Assess the morphology of the erythrocytes.
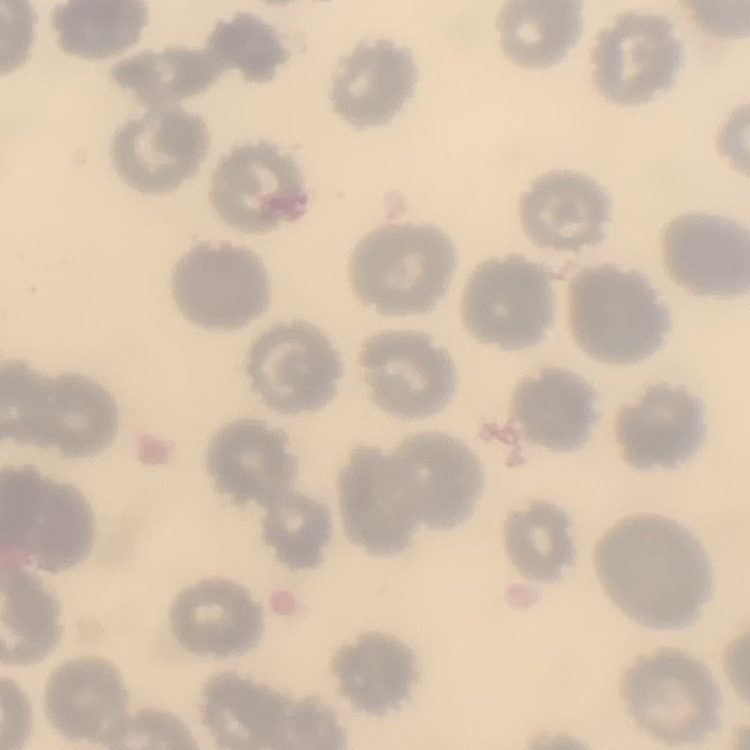

No rouleaux formation.

stain = Field's or Giemsa
image type = square crop of a larger photomicrograph
preparation = thin blood film